Assess this cell for malaria.
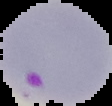

Parasitized.

Image is 112×106 pixels. Segmented cell region on a black background. From a thin blood smear.